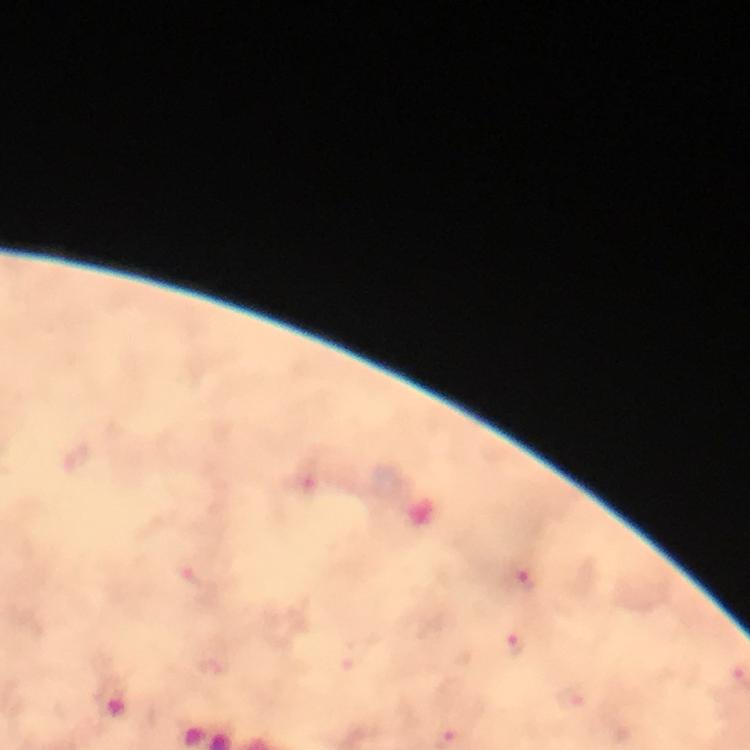

Approximate centers as (x, y) in pixels. Plasmodium parasite locations: (525, 582), (515, 647). Immersion oil applied. From a diagnostic examination for malaria. Photographed with a smartphone mounted on the microscope. Cropped region of a single field of view. Thick smear. Image is 750×750 pixels. Giemsa stain. At 100x magnification.